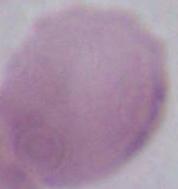 Photomicrograph. A red blood cell is seen. 1000x magnification.